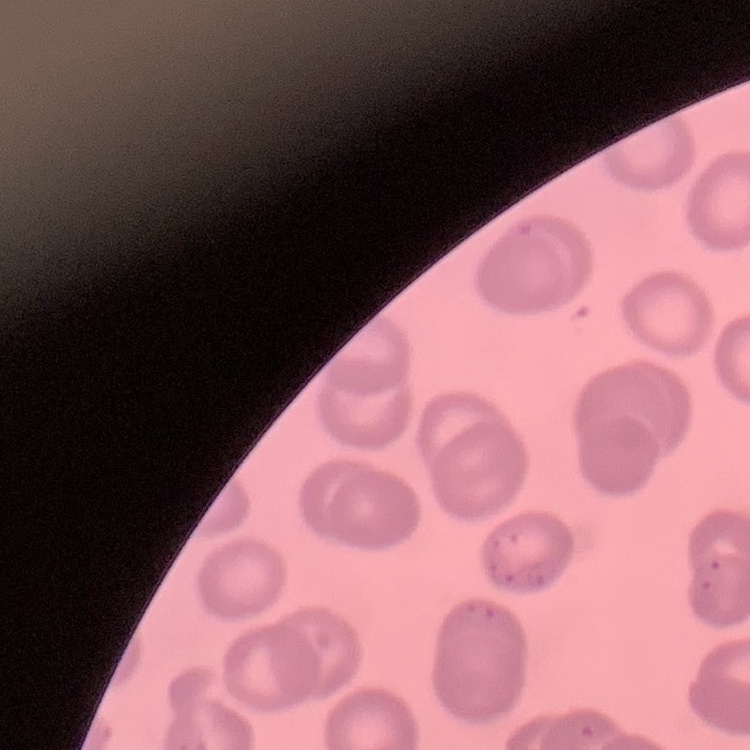 The erythrocytes exhibit no rouleaux formation. Field's or Giemsa stain. Thin peripheral smear. Square crop of a larger photomicrograph.